Identify the blood parasite species.
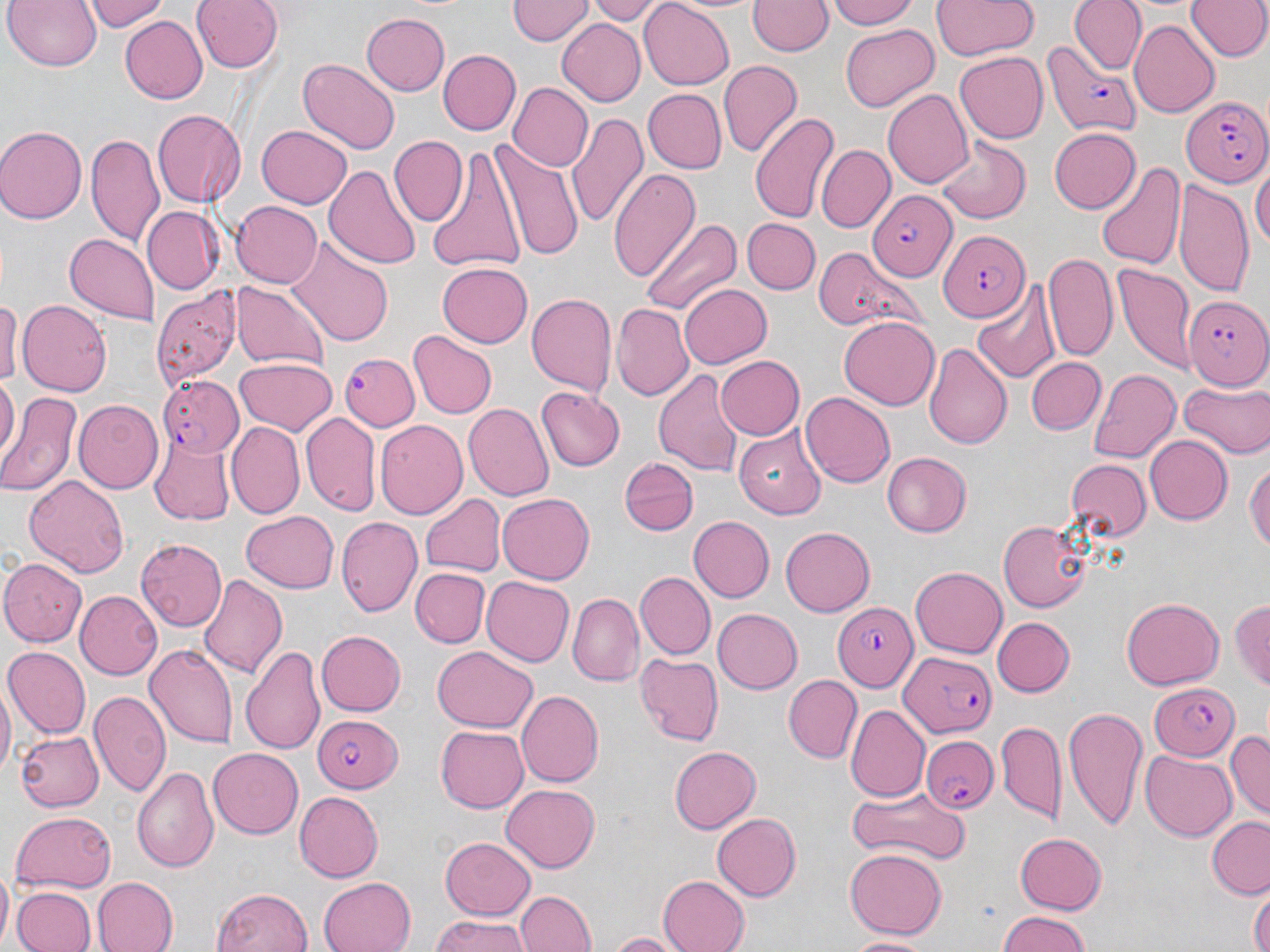

Plasmodium falciparum.

Summary:
  - Coordinate format: approximate bounding boxes as (x1, y1, x2, y2) in pixels
  - Plasmodium falciparum-infected red blood cell locations: (1048, 42, 1141, 132), (1181, 97, 1270, 187), (870, 183, 960, 291), (939, 227, 1031, 320), (1184, 297, 1270, 391), (339, 353, 418, 431), (154, 375, 243, 459), (836, 604, 918, 690), (900, 653, 994, 735), (1148, 681, 1239, 760), (311, 714, 403, 789), (921, 732, 1000, 812)
  - Uninfected red blood cell locations: (5, 0, 102, 71), (84, 0, 169, 32), (192, 0, 282, 73), (586, 0, 664, 24), (825, 0, 919, 29), (932, 0, 1037, 59), (1185, 0, 1269, 61), (507, 1, 592, 46), (640, 1, 735, 90), (748, 1, 831, 58), (1068, 2, 1145, 73), (529, 3, 632, 72), (360, 11, 451, 94), (120, 16, 207, 105), (1129, 19, 1221, 116), (556, 20, 648, 107), (840, 24, 938, 112), (438, 50, 521, 137), (955, 52, 1048, 143), (298, 58, 398, 154), (718, 61, 800, 156), (507, 82, 591, 172), (883, 88, 974, 191), (644, 89, 726, 174), (152, 109, 247, 207), (748, 111, 839, 222), (570, 112, 648, 230), (256, 123, 352, 210), (0, 126, 85, 223), (1049, 128, 1140, 214), (937, 131, 1033, 221), (87, 136, 163, 245), (389, 136, 467, 227), (491, 139, 584, 262), (816, 146, 894, 234), (426, 149, 523, 274), (1095, 161, 1185, 271), (1253, 163, 1270, 252), (325, 164, 422, 271), (610, 167, 698, 279), (1175, 179, 1255, 298), (231, 200, 324, 288), (142, 205, 224, 293), (638, 215, 741, 315), (743, 218, 819, 294), (65, 233, 161, 324), (288, 241, 393, 347), (813, 244, 921, 335), (1044, 253, 1117, 360), (438, 261, 533, 346), (1113, 263, 1193, 372), (974, 280, 1061, 382), (232, 283, 328, 370), (677, 284, 772, 370), (153, 289, 240, 385), (1, 293, 18, 395), (527, 294, 619, 395), (18, 299, 111, 396), (612, 304, 693, 399), (837, 316, 940, 409), (408, 332, 495, 419), (923, 343, 1012, 448), (716, 355, 805, 438), (1026, 356, 1105, 435), (235, 357, 336, 437), (653, 368, 744, 476), (1090, 368, 1181, 462), (0, 375, 18, 465), (1178, 379, 1270, 458), (535, 387, 624, 471), (2, 391, 81, 495), (802, 392, 895, 489), (74, 400, 163, 492), (465, 402, 557, 500), (300, 414, 380, 516), (375, 421, 466, 521), (225, 422, 303, 520), (735, 426, 827, 518), (150, 436, 234, 523), (1145, 437, 1232, 524), (882, 452, 972, 537), (622, 455, 700, 537), (1246, 455, 1270, 563), (1064, 461, 1151, 543), (23, 473, 129, 575), (420, 492, 506, 576), (498, 492, 593, 585), (239, 511, 339, 594), (337, 516, 422, 617), (690, 516, 774, 603), (996, 518, 1090, 613), (780, 526, 875, 617), (136, 539, 227, 632), (0, 560, 101, 652), (910, 565, 1007, 659), (412, 568, 489, 647), (634, 571, 715, 660), (197, 572, 289, 681), (481, 576, 575, 666), (75, 591, 163, 679), (569, 593, 641, 685), (1121, 596, 1224, 689), (1231, 597, 1270, 693), (711, 608, 802, 693), (994, 617, 1074, 696), (316, 630, 406, 715), (146, 644, 237, 748), (4, 646, 91, 737), (240, 646, 329, 755), (432, 647, 537, 732), (636, 653, 725, 746), (783, 674, 861, 762), (0, 686, 14, 779), (90, 688, 168, 797), (517, 690, 604, 787), (847, 704, 931, 802), (1062, 705, 1149, 830), (998, 721, 1067, 820), (435, 724, 529, 814), (16, 730, 102, 812), (1227, 730, 1270, 818), (669, 746, 762, 834), (209, 747, 307, 838), (1141, 750, 1236, 841), (134, 764, 220, 873), (502, 784, 599, 872), (844, 786, 969, 865), (295, 791, 383, 882), (9, 810, 118, 890), (711, 812, 800, 902), (1207, 815, 1270, 897), (1014, 832, 1108, 912), (440, 836, 535, 919), (843, 847, 949, 939), (0, 872, 14, 947), (316, 876, 415, 952), (656, 876, 750, 952), (90, 877, 178, 952), (1249, 883, 1268, 952), (12, 887, 94, 952), (212, 889, 312, 952), (515, 889, 595, 952), (993, 911, 1095, 952), (427, 914, 532, 952), (606, 932, 690, 952), (840, 934, 937, 950)
  - Modality: optical microscopy
  - Field of view: one of a larger specimen
  - Stain: May-Grünwald-Giemsa
  - Magnification: 1000x
  - Preparation: thin blood film
  - Image size: 1270×952 pixels